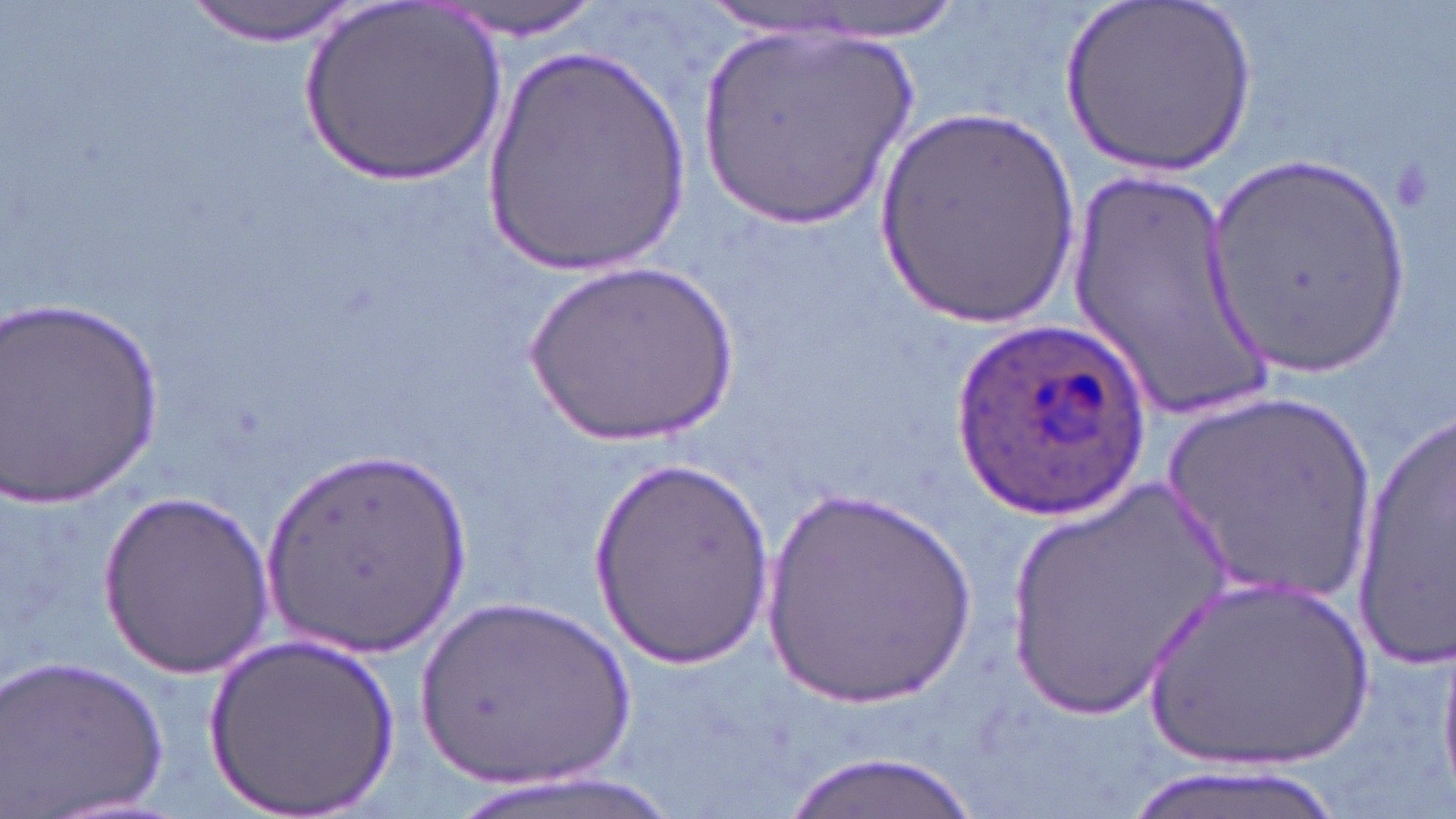
Summary:
  - Coordinate format: approximate bounding boxes as (x1,y1)-(x2,y2) corner pairs in pixels
  - Uninfected red blood cell locations: (184,0)-(360,44), (433,0)-(607,39), (1065,0)-(1260,173), (299,2)-(511,192), (692,21)-(928,237), (478,43)-(698,278), (872,105)-(1081,331), (1201,157)-(1417,379), (1067,173)-(1256,417), (524,264)-(742,452), (1,293)-(167,505), (1157,391)-(1379,612), (1351,402)-(1456,674), (260,448)-(476,658), (590,459)-(776,672), (999,480)-(1235,722), (756,484)-(985,717), (98,485)-(274,677), (1133,574)-(1385,778), (415,596)-(649,788), (203,634)-(406,817), (1439,649)-(1456,796), (3,653)-(169,815), (785,751)-(979,818), (1110,761)-(1356,819)
  - Plasmodium ovale-infected red blood cell locations: (950,319)-(1149,520)
  - Slide-level diagnosis: Plasmodium ovale
  - Image size: 1456×819 pixels
  - Preparation: thin blood film
  - Stain: May-Grünwald-Giemsa
  - Magnification: 1000x
  - Field of view: single
  - Modality: optical microscopy